Assess the morphology of the erythrocytes.
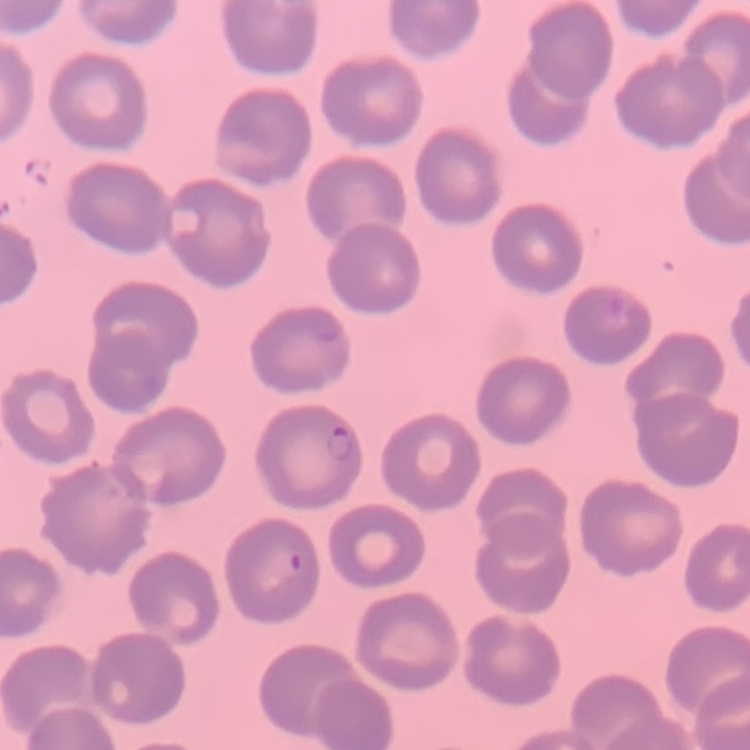
No rouleaux formation.

One tile cut from a larger photomicrograph. Thin peripheral smear. Field's or Giemsa stain.